Report the malaria status of this cell.
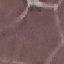

It is uninfected.

Automatically extracted cell patch, resized to 64 × 64 pixels. Acquired by smartphone through the microscope eyepiece. Thin smear of blood. Giemsa stain.